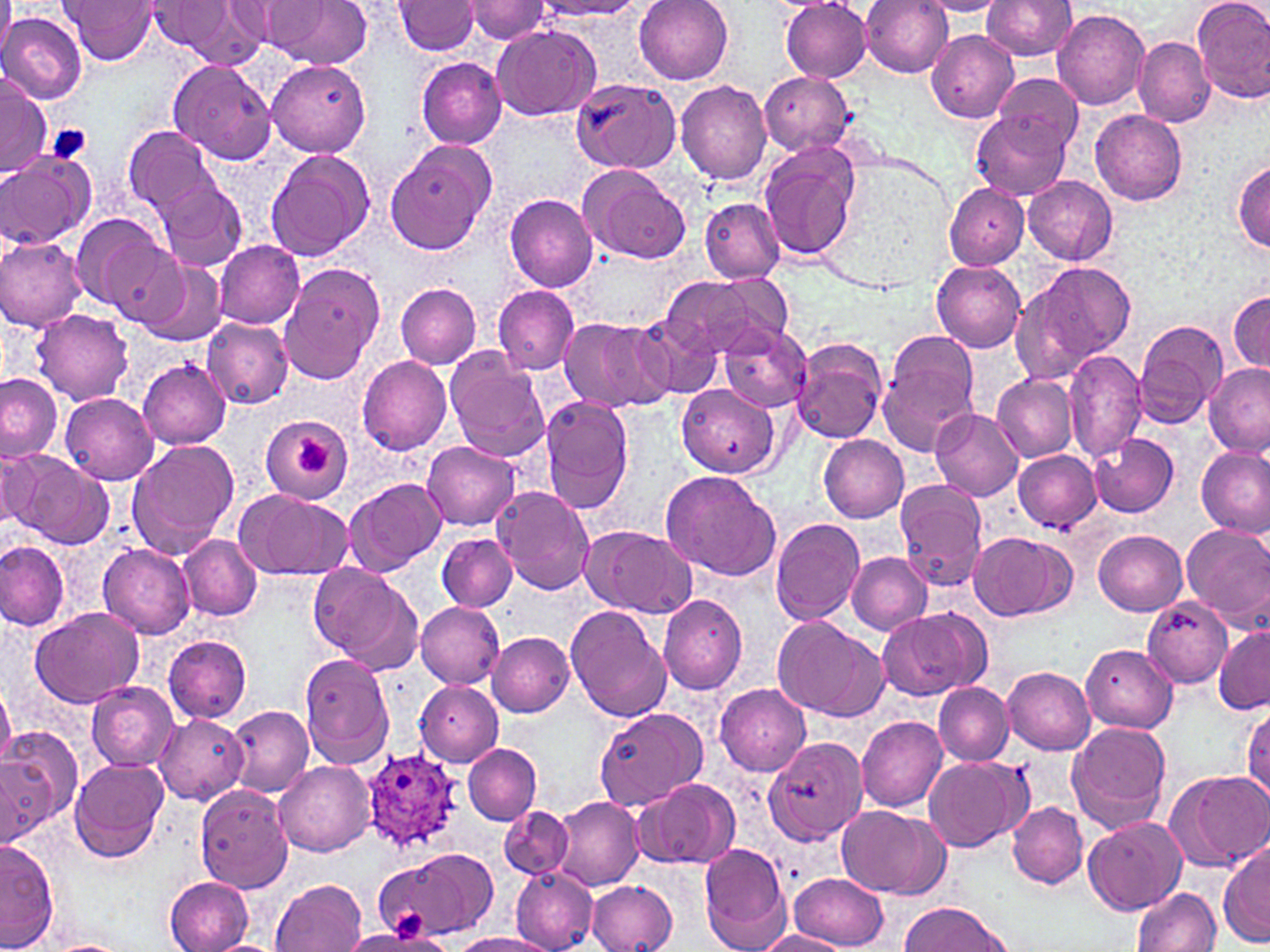

Summary:
  - Coordinate format: approximate bounding boxes as (x1, y1, x2, y2) in pixels
  - Plasmodium ovale-infected red blood cell locations: (359, 749, 463, 854)
  - Uninfected red blood cell locations: (0, 0, 15, 64), (60, 0, 161, 64), (228, 0, 325, 50), (272, 0, 372, 69), (633, 0, 735, 85), (862, 0, 954, 77), (1191, 0, 1270, 103), (158, 1, 268, 65), (393, 1, 481, 55), (467, 1, 551, 43), (536, 1, 644, 19), (918, 1, 1008, 16), (982, 1, 1077, 61), (781, 2, 873, 81), (1052, 6, 1150, 110), (1, 11, 87, 105), (491, 24, 602, 120), (926, 29, 1018, 123), (1134, 37, 1215, 127), (416, 56, 508, 150), (169, 59, 277, 165), (267, 59, 371, 156), (760, 71, 856, 156), (993, 73, 1080, 155), (0, 74, 51, 180), (569, 78, 680, 175), (676, 79, 772, 186), (972, 108, 1071, 201), (1089, 110, 1188, 206), (124, 124, 216, 214), (385, 143, 493, 256), (758, 143, 861, 262), (264, 149, 376, 260), (0, 153, 93, 249), (1232, 159, 1269, 251), (576, 164, 689, 262), (1024, 175, 1118, 265), (157, 179, 246, 271), (944, 184, 1028, 269), (504, 193, 597, 291), (700, 198, 784, 282), (69, 214, 173, 315), (0, 236, 87, 331), (99, 238, 191, 327), (213, 240, 305, 328), (138, 261, 226, 347), (931, 261, 1026, 353), (1017, 262, 1135, 379), (279, 264, 385, 384), (700, 269, 789, 345), (659, 276, 754, 359), (395, 283, 482, 368), (493, 285, 580, 374), (1227, 289, 1270, 376), (31, 309, 134, 405), (629, 314, 722, 401), (200, 316, 292, 410), (559, 317, 663, 412), (1134, 318, 1228, 427), (718, 323, 812, 412), (876, 329, 981, 450), (792, 338, 888, 443), (444, 348, 550, 462), (1063, 350, 1147, 462), (356, 355, 453, 454), (137, 358, 233, 448), (1202, 362, 1269, 453), (0, 373, 63, 462), (993, 374, 1078, 463), (677, 384, 780, 479), (59, 392, 159, 486), (539, 397, 634, 514), (932, 408, 1023, 500), (261, 416, 351, 504), (1088, 432, 1179, 517), (817, 435, 909, 521), (125, 439, 239, 558), (423, 441, 521, 530), (1196, 445, 1270, 538), (1, 447, 51, 532), (1013, 449, 1101, 530), (11, 455, 114, 549), (660, 470, 780, 581), (343, 478, 445, 575), (894, 482, 989, 591), (493, 486, 596, 596), (232, 490, 352, 581), (770, 516, 865, 625), (1181, 523, 1270, 625), (580, 525, 698, 617), (1093, 531, 1188, 615), (967, 532, 1072, 621), (438, 533, 516, 610), (180, 535, 262, 622), (0, 540, 70, 632), (98, 544, 195, 638), (846, 551, 932, 635), (310, 564, 422, 673), (658, 594, 749, 694), (1142, 597, 1233, 688), (414, 602, 505, 687), (565, 605, 671, 722), (30, 606, 144, 708), (877, 608, 987, 702), (772, 617, 886, 721), (1213, 627, 1269, 715), (487, 632, 575, 717), (164, 636, 251, 722), (1081, 643, 1178, 733), (300, 653, 394, 769), (1004, 666, 1096, 753), (87, 681, 179, 770), (415, 681, 503, 766), (0, 682, 14, 771), (714, 682, 812, 776), (933, 682, 1014, 766), (1243, 702, 1270, 805), (224, 704, 313, 798), (594, 708, 707, 811), (153, 712, 247, 804), (856, 715, 948, 811), (1065, 721, 1174, 835), (1, 727, 82, 830), (763, 734, 868, 845), (463, 744, 541, 824), (0, 754, 53, 843), (922, 756, 1029, 851), (69, 759, 168, 862), (274, 760, 375, 856), (1165, 768, 1270, 872), (632, 779, 740, 872), (195, 786, 291, 893), (549, 796, 643, 892), (1007, 801, 1087, 887), (835, 804, 950, 898), (498, 806, 574, 881), (1083, 816, 1187, 915), (1, 840, 58, 951), (1219, 842, 1269, 947), (698, 843, 789, 949), (375, 847, 497, 940), (509, 867, 598, 952), (790, 872, 889, 950), (166, 876, 254, 952), (270, 878, 367, 952), (587, 880, 677, 951), (1133, 886, 1222, 952), (899, 902, 1012, 950), (755, 930, 848, 952), (450, 933, 554, 952), (40, 938, 131, 952), (205, 939, 281, 952)
  - Platelet locations: (49, 123, 92, 163), (293, 435, 333, 477)
  - Slide-level diagnosis: Plasmodium ovale
  - Image size: 1270×952 pixels
  - Preparation: thin blood smear
  - Modality: optical microscopy
  - Stain: May-Grünwald-Giemsa
  - Field of view: single
  - Magnification: 1000x